Give the extent of all Plasmodium ovale-infected red blood cells.
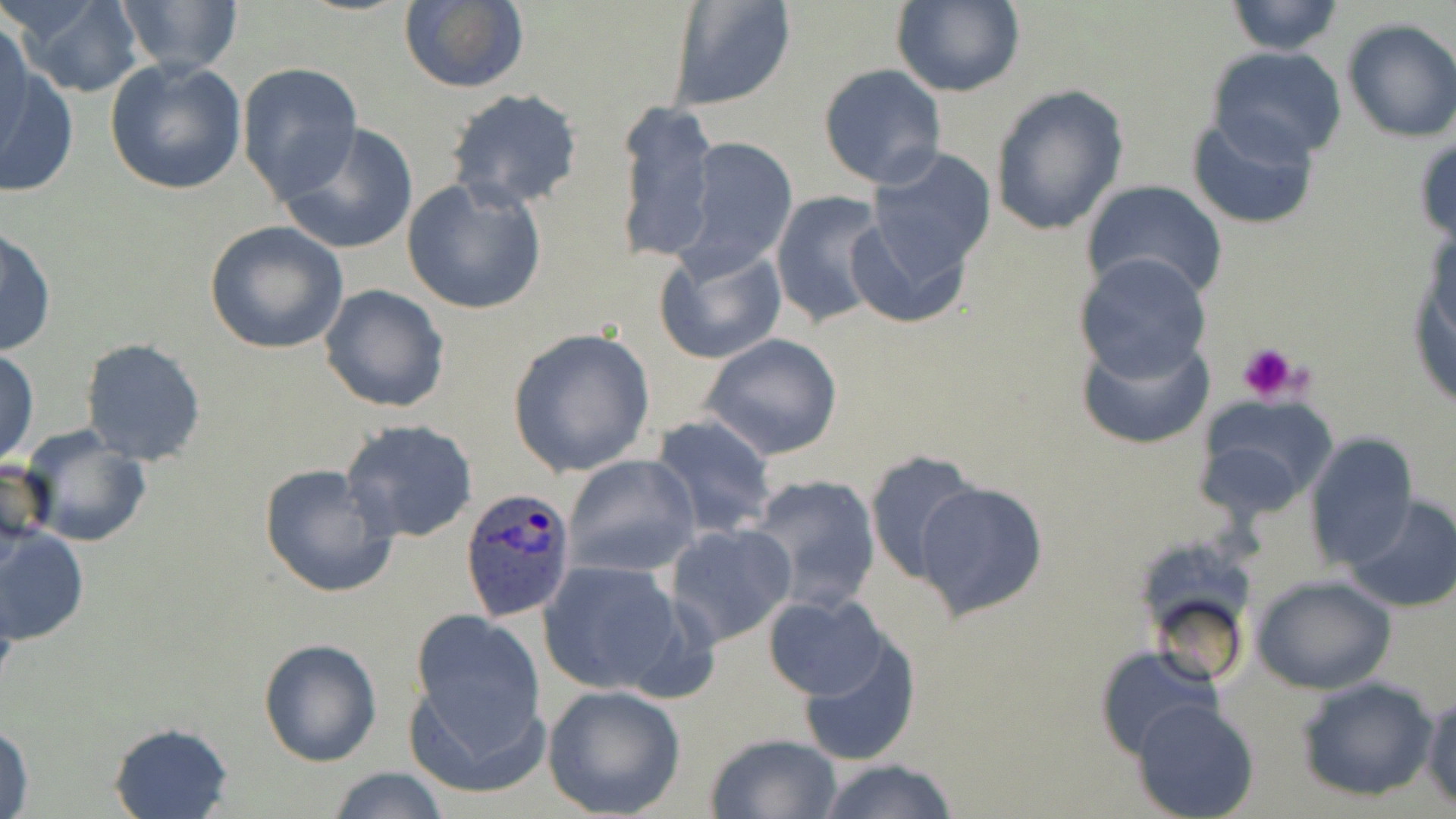

Approximate bounding boxes as [x1, y1, x2, y2] in pixels.
Plasmodium ovale-infected red blood cells: [458, 488, 577, 621].

Platelet locations: [1236, 342, 1298, 402]. Uninfected red blood cell locations: [15, 0, 145, 97], [111, 0, 244, 77], [398, 0, 529, 94], [665, 0, 798, 111], [893, 0, 1023, 98], [1223, 1, 1347, 56], [0, 17, 33, 145], [1340, 17, 1456, 142], [1205, 46, 1351, 168], [104, 58, 248, 197], [0, 63, 79, 200], [238, 63, 362, 201], [818, 63, 946, 189], [988, 85, 1129, 237], [444, 88, 584, 211], [614, 100, 718, 265], [1184, 110, 1319, 231], [276, 122, 418, 255], [1412, 132, 1456, 250], [677, 137, 798, 275], [861, 146, 997, 293], [401, 179, 548, 314], [1080, 179, 1226, 301], [770, 190, 890, 331], [1406, 206, 1455, 421], [204, 222, 349, 355], [1, 226, 56, 357], [654, 243, 787, 365], [1073, 251, 1212, 380], [319, 284, 451, 414], [1079, 322, 1215, 450], [507, 325, 657, 478], [700, 332, 843, 461], [79, 338, 206, 466], [0, 348, 39, 469], [1191, 396, 1336, 516], [650, 414, 778, 539], [341, 419, 479, 543], [21, 428, 153, 549], [1302, 433, 1418, 570], [863, 450, 980, 585], [0, 454, 52, 557], [562, 454, 701, 578], [258, 462, 399, 599], [744, 474, 882, 614], [913, 481, 1049, 620], [1343, 496, 1456, 613], [664, 522, 797, 647], [0, 525, 90, 646], [536, 561, 688, 695], [1252, 575, 1396, 695], [763, 593, 891, 700], [408, 609, 551, 781], [799, 634, 921, 767], [257, 636, 383, 767], [1095, 645, 1219, 762], [1295, 673, 1439, 803], [542, 684, 687, 818], [1422, 691, 1456, 808], [1131, 698, 1259, 819], [0, 720, 35, 819], [108, 721, 235, 819], [705, 733, 843, 818], [816, 757, 960, 819], [327, 766, 452, 818]. Slide-level diagnosis: Plasmodium ovale. May-Grünwald-Giemsa-stained preparation. Light microscopy. Single field of view. Image is 1456×819 pixels. Thin blood smear. Captured at 1000x magnification.